Classify this cell by malaria status.
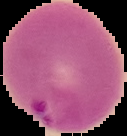
Parasitized.

image_size: 127×136 pixels
image_type: segmented cell region with the area outside set to black
preparation: thin blood smear